Name the parasite shown.
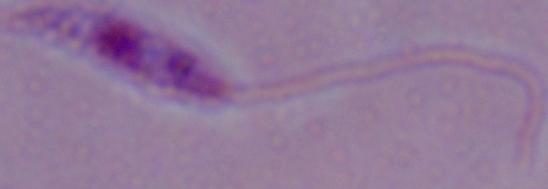
Leishmania.

Photomicrograph. 1000x magnification.